Assess this cell for malaria.
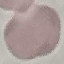
It is uninfected.

Cell patch, automatically extracted from a larger field of view and resized to 64 × 64 pixels. Thin blood film. Giemsa-stained preparation. Photographed with a smartphone camera at the microscope eyepiece.